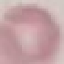

Result: negative for malaria parasites. Giemsa stain. Thin blood film. Acquired by smartphone through the microscope eyepiece. Cell patch, automatically extracted from a larger field of view and resized to 64 × 64 pixels.